Assess the morphology of the erythrocytes.
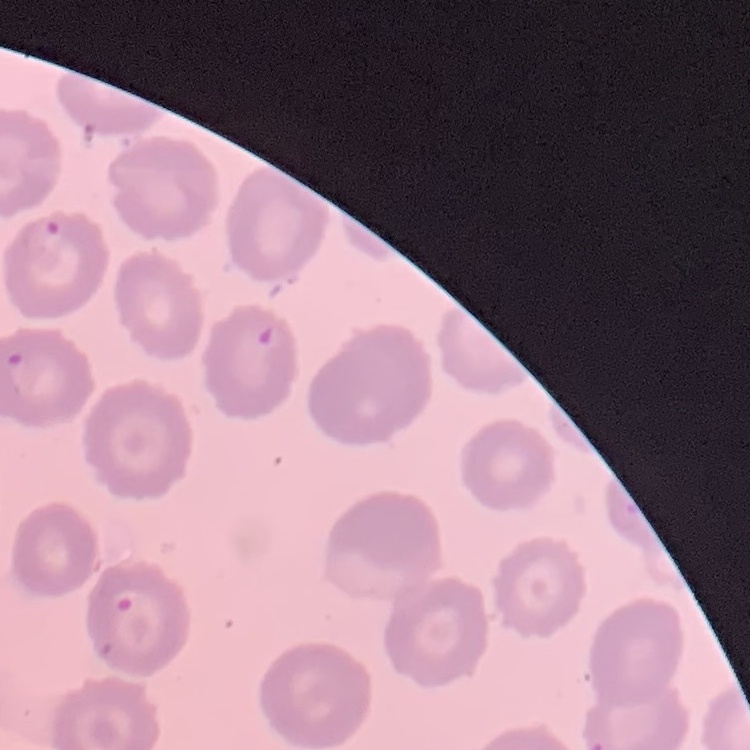
No rouleaux formation.

Summary:
  - Preparation: thin blood smear
  - Image type: one tile cut from a larger photomicrograph
  - Stain: Field's or Giemsa